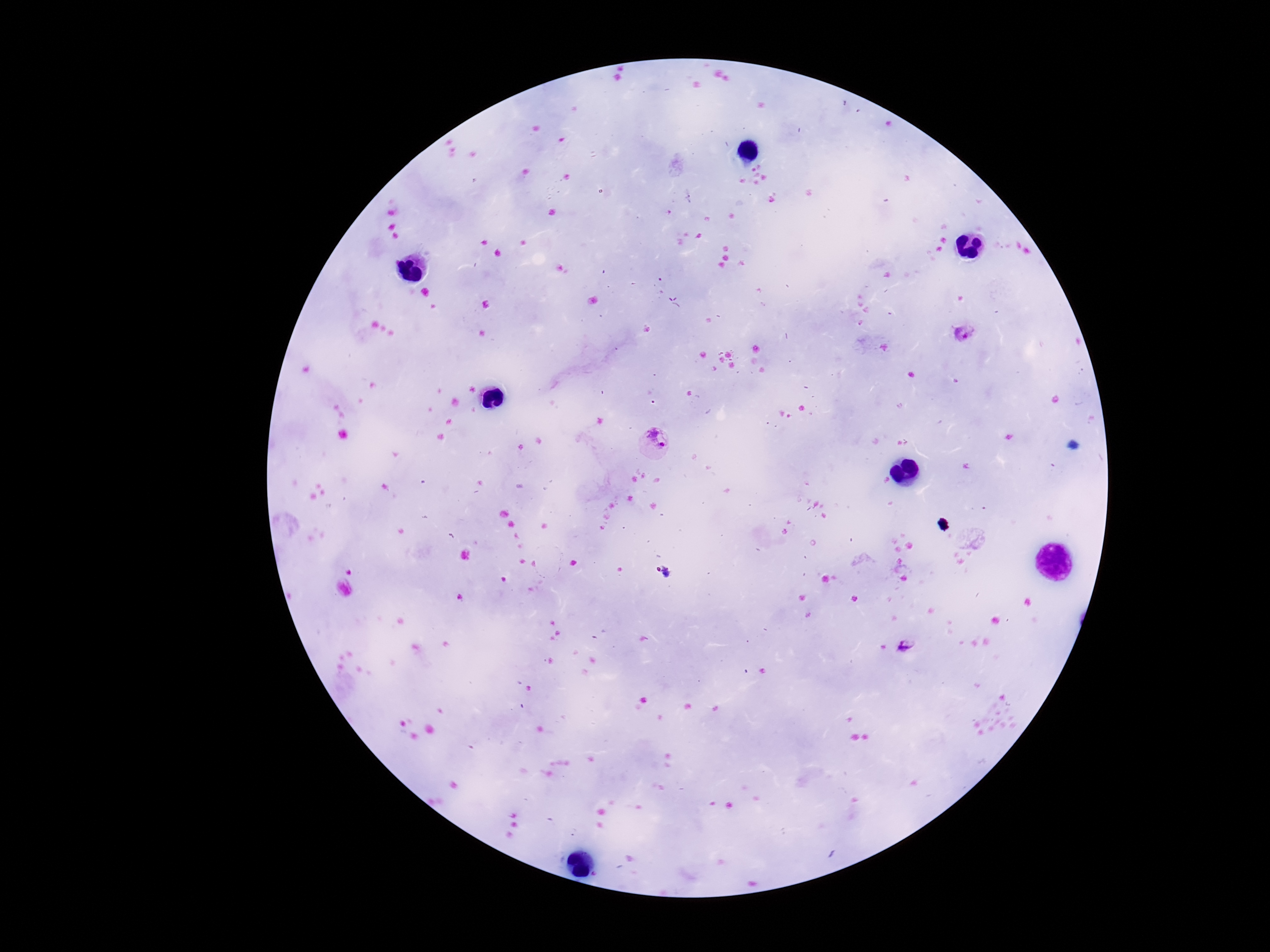
{
  "preparation": "thick peripheral-blood smear",
  "image_size": "1270×952 pixels",
  "plasmodium_parasite_locations": "approximate centers as (x, y) in pixels: (964, 333), (654, 441), (665, 572), (907, 645)",
  "field_of_view": "one from this slide",
  "magnification": "100x",
  "patient_malaria_status": "positive",
  "capture": "smartphone camera through the microscope eyepiece",
  "stain": "Giemsa"
}